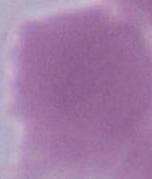

identification = red blood cell
modality = micrograph
magnification = 1000x